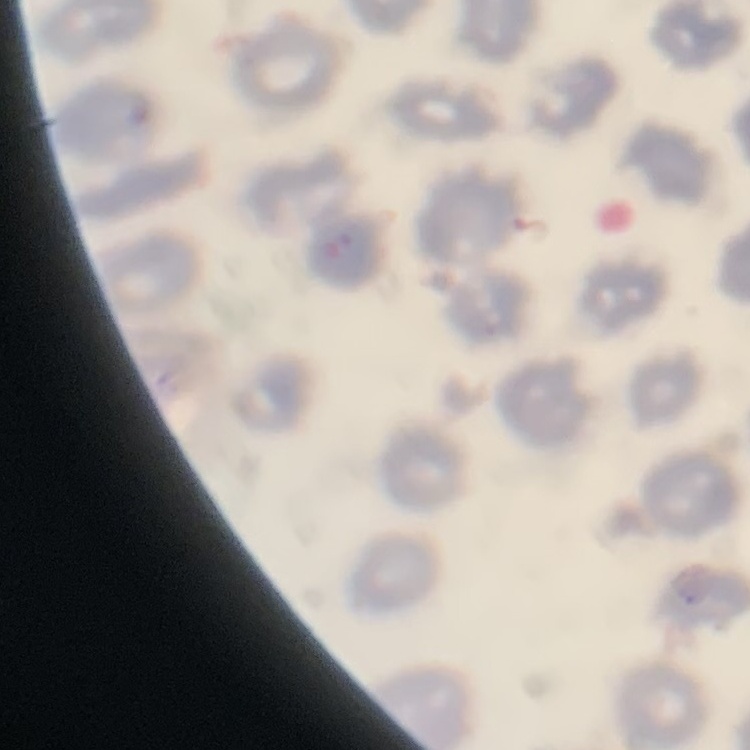

Summary:
  - Erythrocyte morphology: no rouleaux formation
  - Image type: square crop of a larger photomicrograph
  - Stain: Field's or Giemsa
  - Preparation: thin blood film